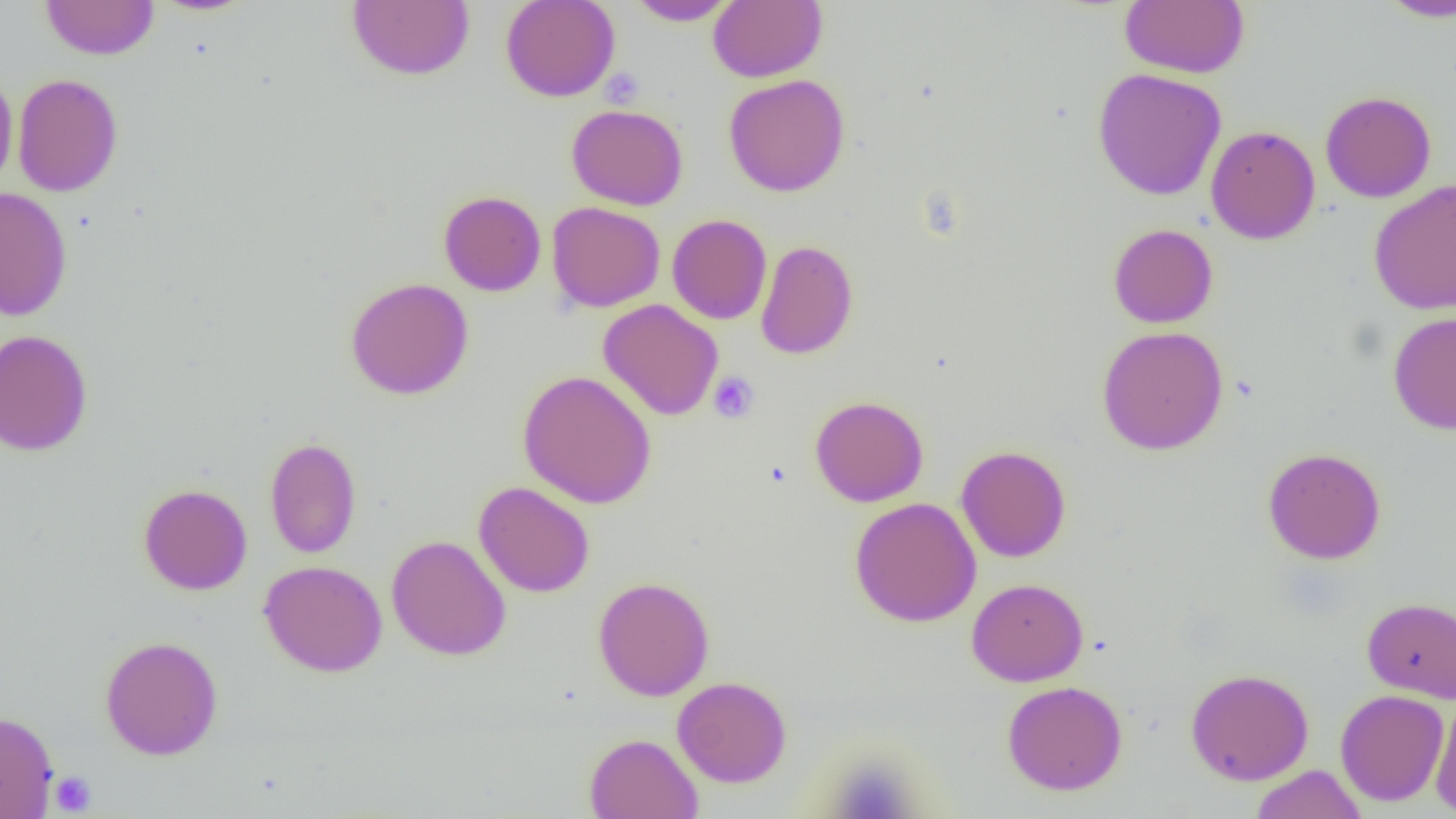 Approximate bounding boxes as [x1, y1, x2, y2] in pixels. Uninfected red blood cell locations: [41, 0, 159, 60], [149, 0, 259, 17], [347, 0, 474, 81], [500, 0, 620, 102], [626, 0, 738, 26], [708, 0, 826, 82], [1119, 0, 1249, 78], [1377, 0, 1456, 22], [1092, 68, 1227, 201], [0, 70, 18, 196], [12, 73, 123, 197], [723, 74, 850, 197], [1320, 91, 1436, 203], [566, 104, 688, 210], [1206, 124, 1320, 244], [1369, 179, 1456, 316], [1, 187, 73, 321], [438, 190, 546, 296], [547, 201, 665, 312], [667, 214, 772, 324], [1108, 223, 1218, 328], [755, 240, 858, 360], [345, 277, 474, 399], [598, 299, 723, 421], [1388, 311, 1456, 435], [1097, 325, 1228, 455], [0, 329, 93, 456], [517, 370, 657, 509], [810, 395, 929, 507], [265, 436, 362, 558], [956, 445, 1071, 562], [1262, 447, 1386, 564], [473, 481, 594, 598], [138, 483, 252, 595], [849, 497, 982, 627], [386, 535, 511, 660], [259, 560, 388, 677], [593, 576, 714, 701], [966, 578, 1088, 686], [1361, 597, 1456, 703], [100, 635, 223, 760], [1185, 667, 1314, 786], [672, 676, 792, 788], [1002, 680, 1128, 796], [1335, 689, 1450, 806], [1430, 693, 1456, 816], [0, 710, 58, 818], [585, 733, 703, 819], [1250, 764, 1368, 819]. Platelet locations: [599, 69, 646, 109], [708, 371, 759, 423], [824, 755, 922, 819], [50, 771, 96, 815]. Slide-level diagnosis: negative for blood parasites. Image is 1456×819 pixels. Optical microscopy. Thin blood film. Single field of view. 1000x magnification.